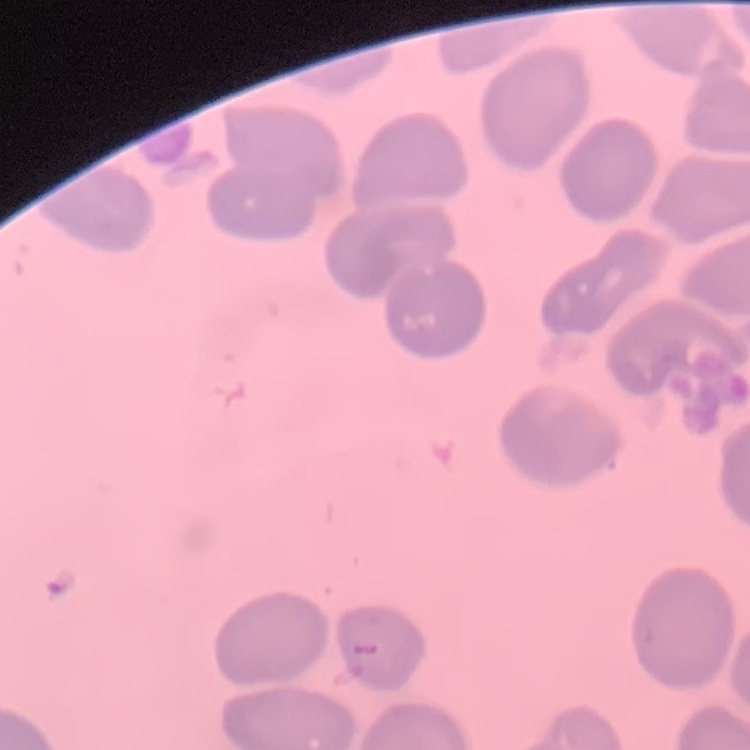

erythrocyte_morphology: no rouleaux formation
stain: Field's or Giemsa
image_type: square crop of a larger photomicrograph
preparation: thin blood film